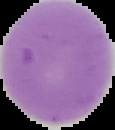
Summary:
  - Result: negative for Plasmodium parasites
  - Image size: 115×130 pixels
  - Image type: cell region segmented out of the field of view; surrounding area masked to black
  - Preparation: thin blood smear